Classify this cell by malaria status.
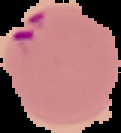
Parasitized.

image_type: segmented cell region on a black background
preparation: thin blood smear
image_size: 121×133 pixels